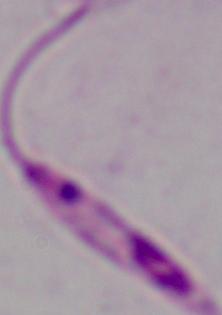

Captured at 1000x magnification. A Leishmania parasite is shown. Micrograph.